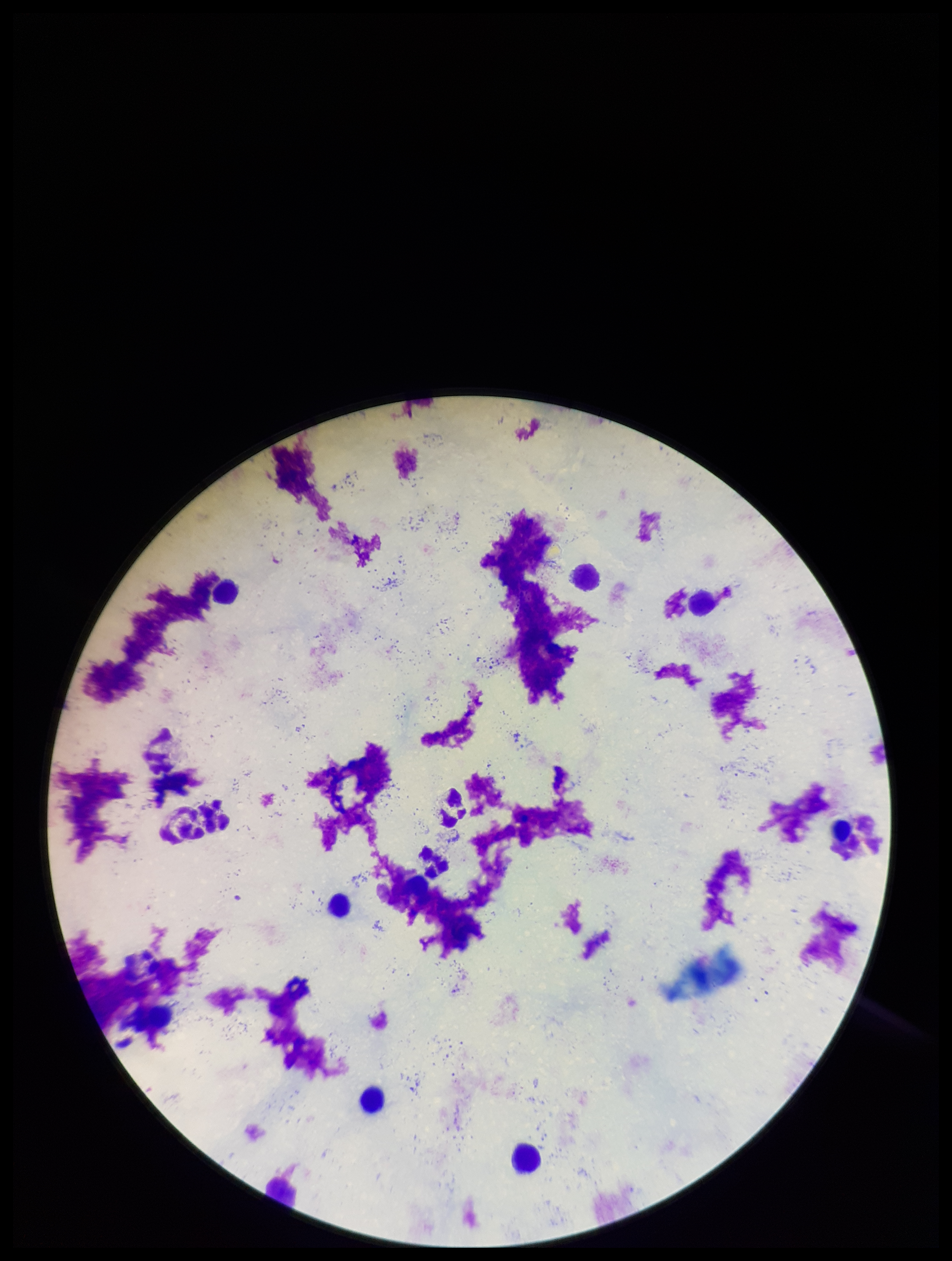 Patient malaria status: negative. Parasite count: 0. Single field of view. Preparation: thick blood smear. Image is 952×1261 pixels. Leukocyte count: 9. Photographed through the microscope eyepiece with a smartphone camera. Plasmodium parasites: none detected. Giemsa stain.